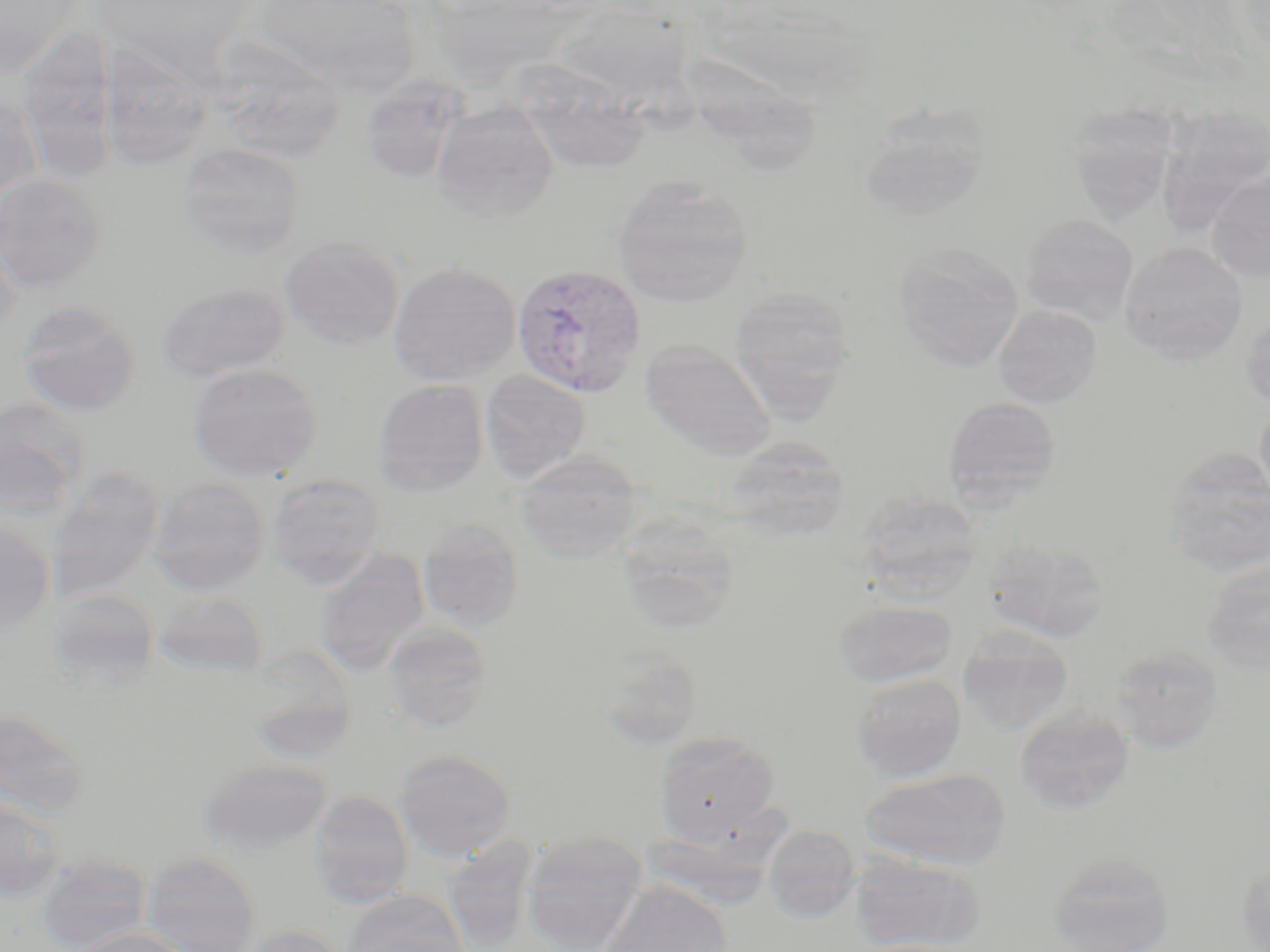 Approximate bounding boxes as (x1, y1, x2, y2) in pixels. Uninfected red blood cell locations: (0, 0, 81, 79), (253, 1, 422, 97), (558, 4, 692, 103), (17, 26, 120, 182), (206, 36, 347, 163), (96, 40, 215, 172), (511, 62, 651, 176), (683, 66, 822, 183), (360, 77, 469, 185), (0, 93, 40, 209), (431, 99, 560, 223), (1065, 104, 1181, 223), (1158, 108, 1269, 231), (857, 113, 989, 223), (176, 141, 306, 258), (1208, 168, 1270, 283), (0, 173, 108, 296), (611, 176, 753, 308), (0, 214, 23, 337), (1021, 214, 1138, 322), (279, 237, 404, 350), (1119, 242, 1248, 363), (893, 244, 1024, 371), (388, 262, 521, 386), (156, 282, 290, 383), (728, 286, 857, 418), (17, 299, 141, 417), (993, 305, 1102, 407), (640, 339, 777, 460), (187, 363, 324, 481), (480, 370, 591, 484), (372, 379, 488, 497), (943, 396, 1061, 506), (0, 397, 91, 515), (1256, 397, 1270, 511), (722, 436, 851, 542), (1162, 447, 1270, 575), (513, 452, 644, 562), (46, 468, 165, 602), (267, 473, 387, 587), (147, 478, 270, 595), (854, 491, 983, 601), (614, 515, 741, 634), (0, 518, 56, 633), (417, 518, 525, 631), (980, 537, 1111, 643), (314, 549, 430, 676), (1201, 559, 1270, 676), (45, 588, 161, 690), (152, 591, 269, 679), (832, 600, 959, 688), (381, 621, 493, 732), (957, 627, 1074, 733), (1107, 644, 1224, 752), (590, 645, 705, 750), (850, 673, 966, 782), (1014, 706, 1135, 815), (0, 707, 91, 821), (652, 730, 781, 844), (394, 749, 517, 861), (198, 759, 332, 855), (859, 768, 1010, 869), (308, 789, 414, 909), (0, 794, 66, 900), (763, 824, 861, 923), (519, 831, 650, 952), (440, 835, 540, 950), (142, 851, 262, 952), (1048, 851, 1176, 952), (37, 854, 151, 952), (849, 854, 985, 951), (1236, 859, 1270, 952), (595, 881, 733, 952), (342, 890, 470, 952), (239, 924, 351, 952), (65, 927, 196, 952), (848, 939, 977, 952). Plasmodium vivax-infected red blood cell locations: (511, 263, 649, 399). Slide-level diagnosis: Plasmodium vivax. One field of a larger specimen. May-Grünwald-Giemsa stain. Captured at 1000x magnification. Thin blood film. Image is 1270×952 pixels. Optical microscopy.